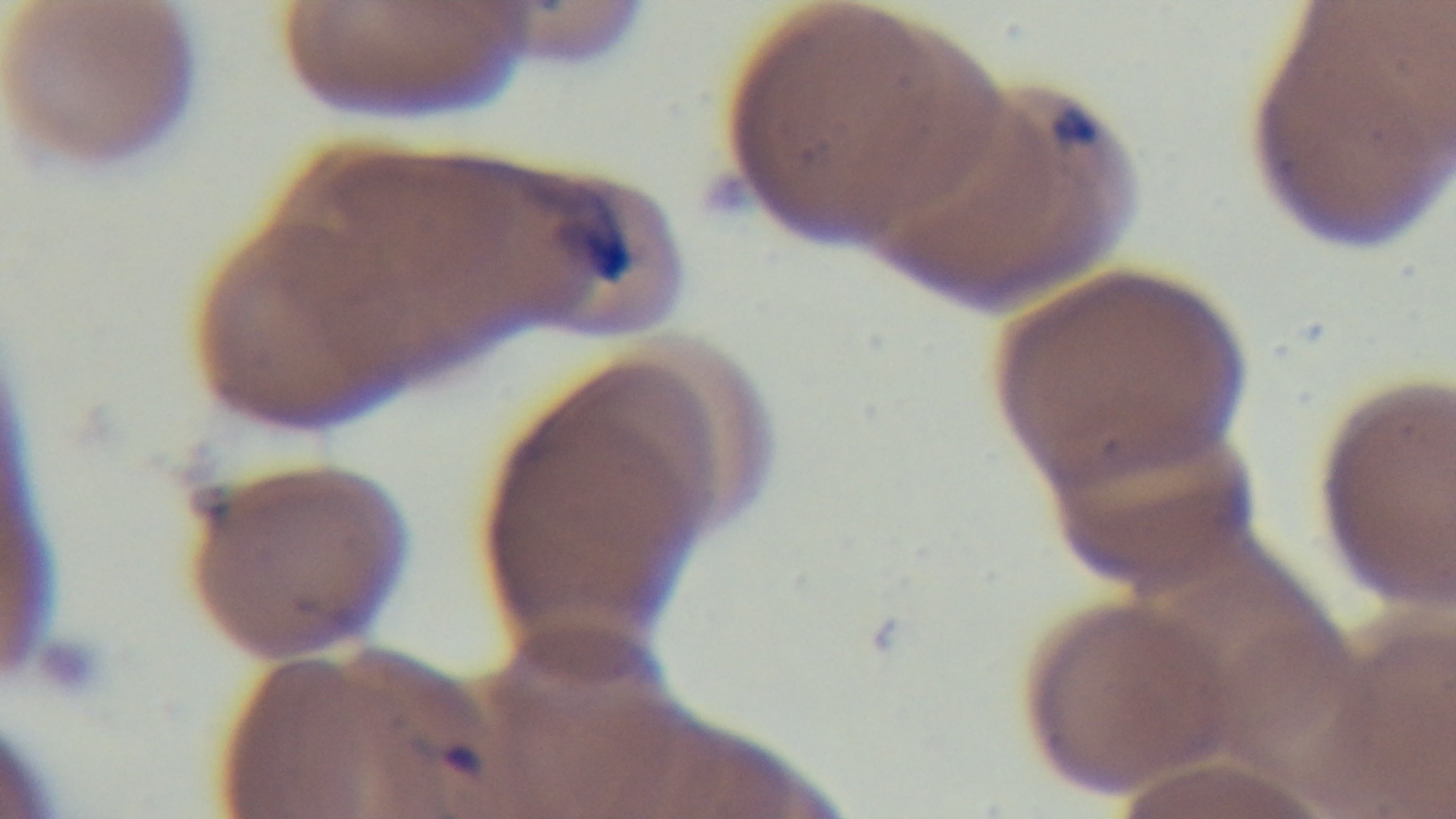

Summary:
  - Field of view: single
  - Modality: light microscopy
  - Malaria status: infected
  - Stain: Giemsa
  - Capture: mounted 4K digital camera
  - Objective: 100x oil immersion
  - Preparation: thin